Classify the preparation.
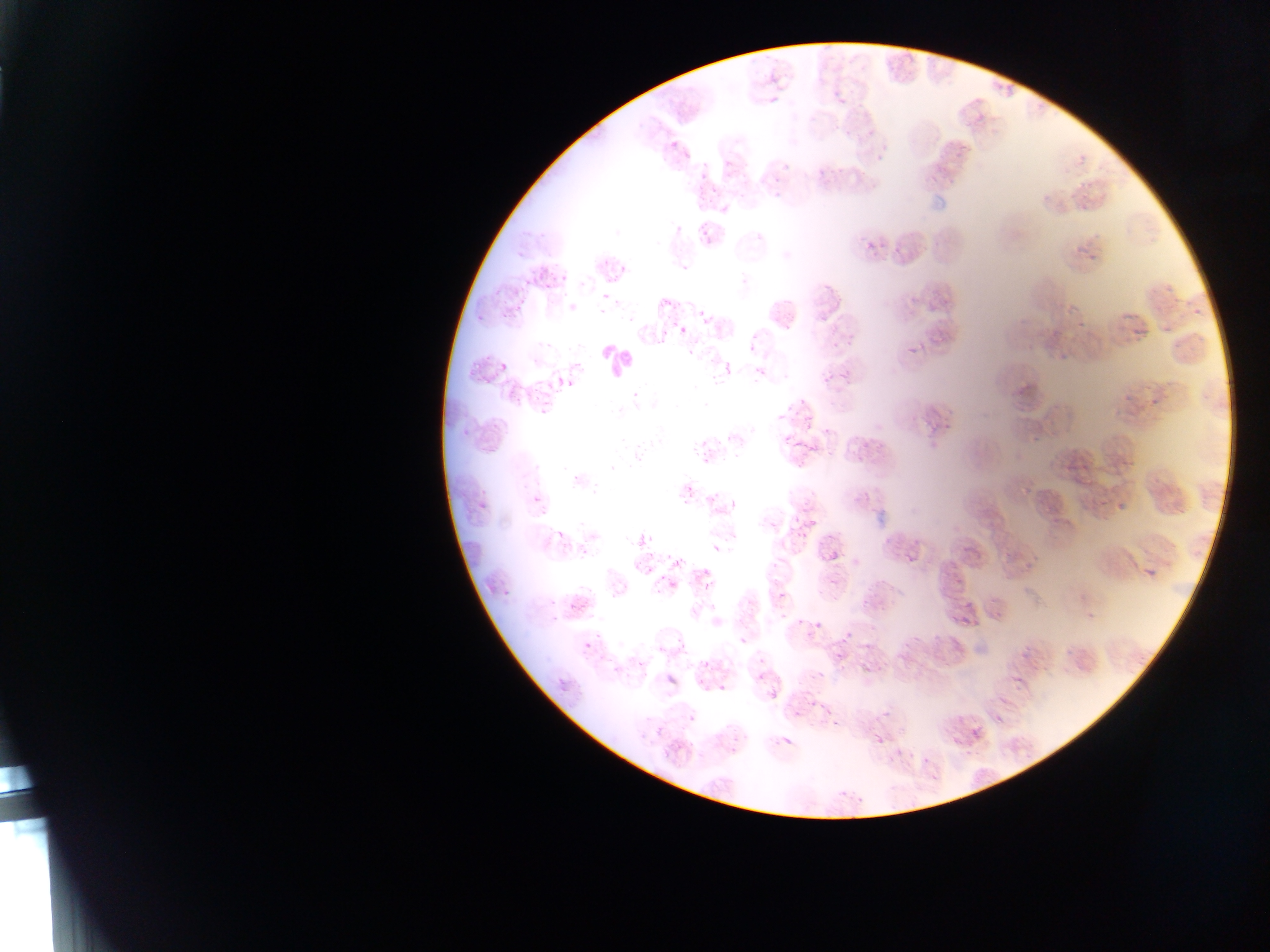

Thin blood smear.

leukocyte locations = approximate bounding boxes as (left, top, right, bottom) in pixels: (599, 343, 638, 383)
Plasmodium parasite locations = approximate bounding boxes as (left, top, right, bottom) in pixels: (764, 88, 783, 102), (667, 138, 681, 153), (616, 264, 631, 275), (767, 295, 801, 335), (1185, 296, 1209, 324), (475, 312, 488, 326), (1072, 312, 1091, 328), (680, 320, 693, 334), (906, 342, 923, 358), (499, 362, 511, 375), (722, 362, 734, 377), (837, 367, 854, 385), (819, 370, 834, 385), (561, 378, 576, 392), (1199, 389, 1220, 415), (1147, 394, 1161, 405), (538, 404, 552, 419), (531, 494, 542, 506), (1087, 497, 1113, 511), (476, 500, 488, 513), (1116, 504, 1126, 510), (713, 544, 721, 553), (827, 549, 841, 563), (1143, 565, 1160, 581), (787, 614, 802, 627), (812, 622, 821, 632), (838, 628, 856, 647), (739, 636, 749, 647), (583, 641, 593, 651), (691, 654, 713, 673), (656, 670, 682, 688), (712, 679, 738, 695), (765, 687, 778, 697), (881, 710, 895, 722), (686, 714, 697, 726), (655, 725, 666, 736), (869, 727, 888, 746), (783, 736, 793, 748)
image size = 1270×952 pixels
capture = mobile-phone photograph through a microscope
country = Ghana
field of view = single